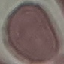

malaria status = uninfected
image type = cell patch, automatically extracted from a larger field of view and resized to 64 × 64 pixels
stain = Giemsa
preparation = thin smear
capture = smartphone camera at the microscope eyepiece